Locate every Plasmodium parasite.
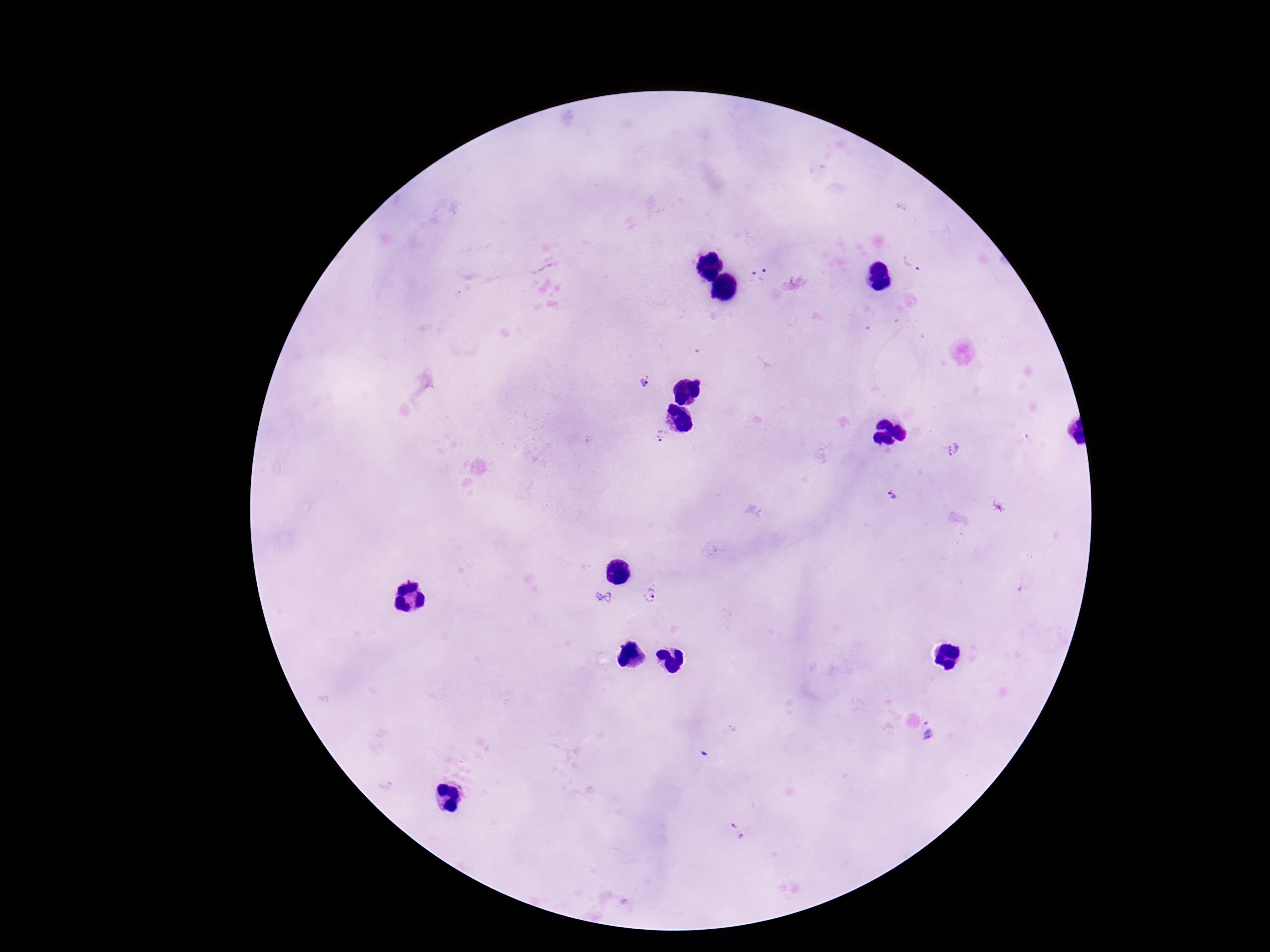

Approximate centers as [x, y] in pixels.
Plasmodium parasites: [913, 261], [766, 276], [748, 278], [644, 382], [659, 434], [953, 448], [893, 496], [603, 597], [654, 600], [932, 733], [739, 832].

magnification = 100x
capture = smartphone camera through the microscope eyepiece
field of view = single
stain = Giemsa
image size = 1270×952 pixels
preparation = thick peripheral-blood smear
patient malaria status = positive